Describe the morphology of the red blood cells.
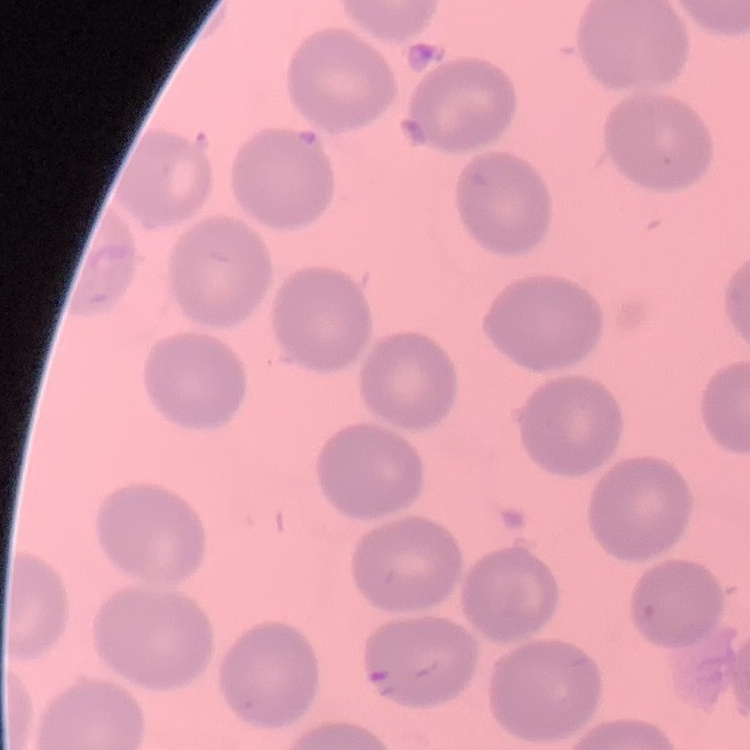
They show no rouleaux formation.

Summary:
  - Preparation: thin blood film
  - Image type: square crop of a larger photomicrograph
  - Stain: Field's or Giemsa